Report the malaria status of this cell.
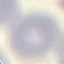

Uninfected.

image type = cell patch, automatically extracted from a larger field of view and resized to 64 × 64 pixels
stain = Giemsa
preparation = thin blood film
capture = smartphone through the microscope eyepiece